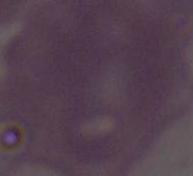
Summary:
  - Modality: photomicrograph
  - Identification: red blood cell
  - Magnification: 1000x